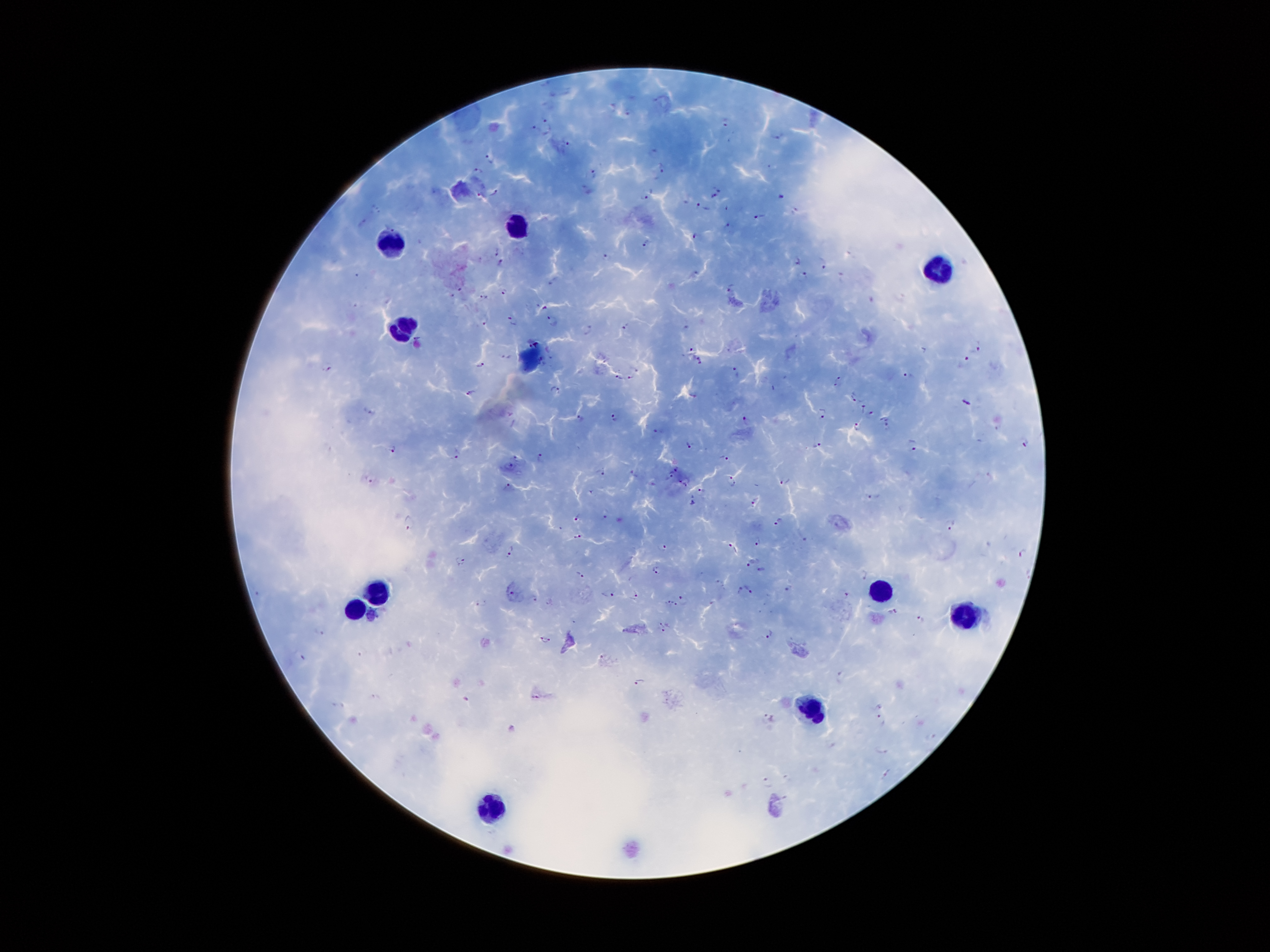

Approximate object centers, in pixels from the top-left corner.
Summary:
  - Plasmodium parasite locations: (x=630, y=111), (x=726, y=123), (x=549, y=125), (x=531, y=131), (x=777, y=136), (x=569, y=144), (x=490, y=158), (x=662, y=170), (x=480, y=172), (x=594, y=173), (x=716, y=186), (x=588, y=190), (x=495, y=192), (x=480, y=195), (x=645, y=198), (x=780, y=198), (x=712, y=199), (x=702, y=207), (x=378, y=208), (x=726, y=208), (x=794, y=211), (x=758, y=216), (x=362, y=224), (x=727, y=225), (x=694, y=236), (x=645, y=243), (x=497, y=251), (x=605, y=255), (x=795, y=261), (x=501, y=262), (x=820, y=263), (x=694, y=271), (x=801, y=273), (x=356, y=275), (x=555, y=279), (x=729, y=285), (x=459, y=289), (x=504, y=290), (x=452, y=296), (x=482, y=298), (x=543, y=307), (x=483, y=319), (x=513, y=321), (x=553, y=321), (x=626, y=325), (x=589, y=331), (x=692, y=349), (x=977, y=349), (x=507, y=356), (x=966, y=358), (x=698, y=360), (x=481, y=365), (x=329, y=368), (x=735, y=372), (x=909, y=376), (x=619, y=377), (x=630, y=378), (x=838, y=380), (x=556, y=389), (x=471, y=392), (x=693, y=394), (x=852, y=394), (x=967, y=404), (x=863, y=408), (x=370, y=412), (x=822, y=412), (x=870, y=412), (x=616, y=417), (x=581, y=418), (x=747, y=419), (x=858, y=426), (x=888, y=427), (x=658, y=432), (x=1025, y=443), (x=816, y=444), (x=913, y=445), (x=689, y=446), (x=394, y=448), (x=454, y=454), (x=540, y=456), (x=724, y=456), (x=516, y=458), (x=509, y=467), (x=676, y=468), (x=602, y=471), (x=635, y=473), (x=671, y=475), (x=370, y=479), (x=732, y=480), (x=685, y=481), (x=785, y=484), (x=701, y=491), (x=592, y=492), (x=874, y=496), (x=693, y=501), (x=757, y=502), (x=605, y=516), (x=577, y=517), (x=779, y=522), (x=409, y=524), (x=952, y=524), (x=577, y=536), (x=806, y=538), (x=758, y=542), (x=732, y=547), (x=665, y=548), (x=510, y=550), (x=1024, y=554), (x=462, y=559), (x=751, y=563), (x=656, y=570), (x=761, y=570), (x=579, y=573), (x=866, y=574), (x=719, y=583), (x=788, y=587), (x=749, y=588), (x=738, y=591), (x=635, y=592), (x=609, y=595), (x=846, y=595), (x=513, y=596), (x=534, y=598), (x=684, y=599), (x=481, y=602), (x=668, y=602), (x=677, y=606), (x=892, y=611), (x=921, y=619), (x=662, y=625), (x=324, y=631), (x=664, y=631), (x=768, y=633), (x=545, y=640), (x=302, y=658), (x=603, y=659), (x=841, y=676), (x=641, y=683), (x=537, y=696), (x=376, y=698), (x=467, y=699), (x=340, y=706), (x=768, y=719), (x=882, y=719), (x=931, y=737), (x=885, y=750), (x=888, y=774), (x=768, y=783)
  - Leukocyte locations: (x=516, y=223), (x=390, y=231), (x=936, y=267), (x=399, y=328), (x=530, y=360), (x=878, y=590), (x=378, y=594), (x=355, y=609), (x=971, y=613), (x=814, y=708), (x=491, y=810)
  - Field of view: single
  - Magnification: 100x
  - Capture: smartphone camera through the microscope eyepiece
  - Patient malaria status: infected with Plasmodium falciparum
  - Preparation: thick blood smear
  - Stain: Giemsa
  - Image size: 1270×952 pixels